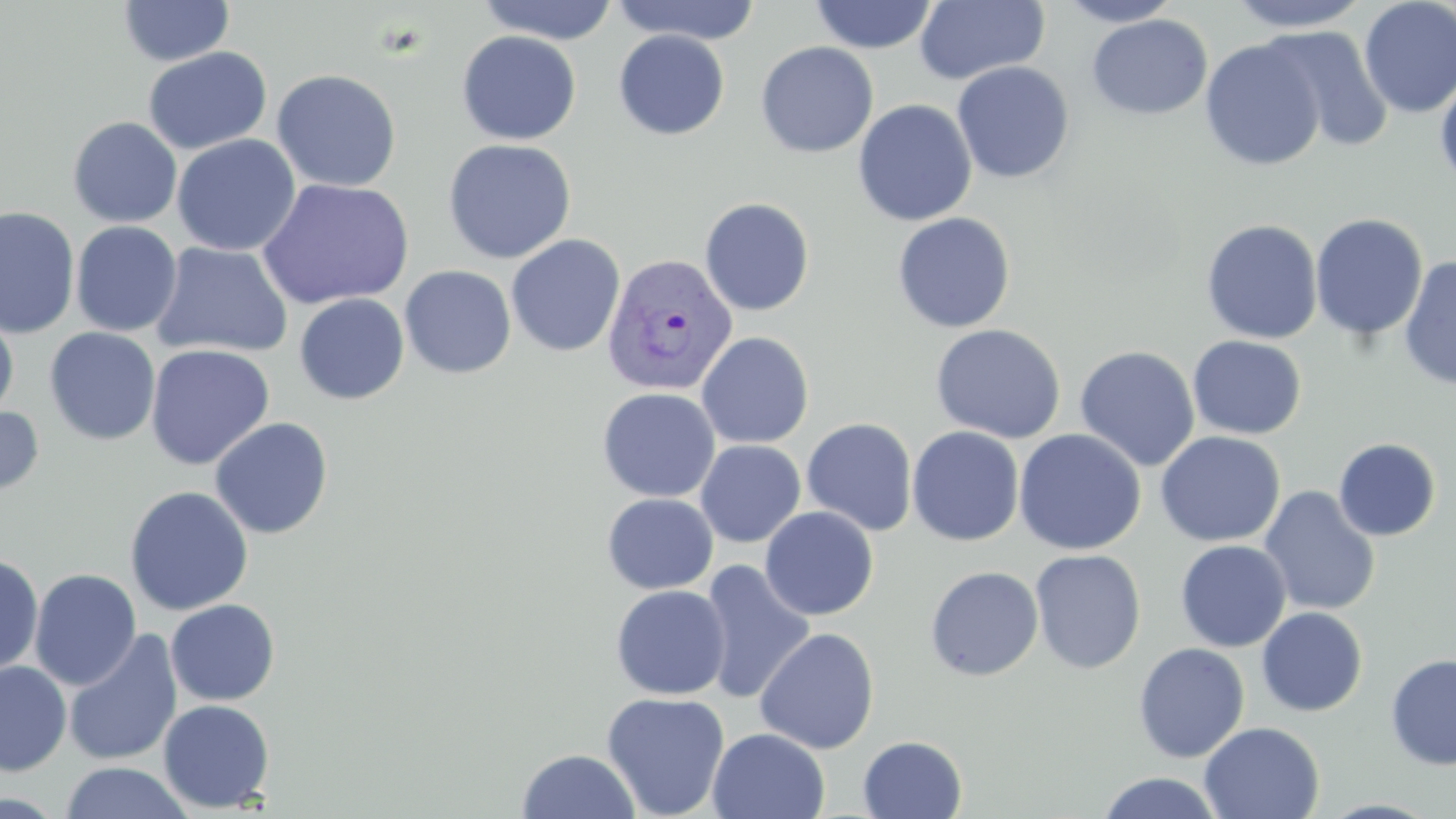 Approximate bounding boxes as (x1,y1)-(x2,y2) corner pairs in pixels. Plasmodium vivax-infected red blood cell locations: (601,251)-(738,397). Uninfected red blood cell locations: (477,0)-(620,45), (809,0)-(938,54), (913,0)-(1051,85), (1054,0)-(1185,27), (1224,0)-(1373,32), (1358,0)-(1456,118), (118,1)-(235,67), (608,1)-(762,45), (1087,14)-(1212,120), (1265,25)-(1394,152), (613,29)-(730,140), (456,30)-(581,146), (1199,38)-(1327,171), (755,41)-(879,158), (143,47)-(272,155), (952,61)-(1075,184), (271,68)-(402,192), (1434,73)-(1456,191), (852,99)-(978,227), (68,116)-(182,228), (172,134)-(300,256), (442,138)-(577,264), (257,178)-(414,310), (699,197)-(815,316), (0,206)-(80,338), (892,212)-(1016,333), (1310,213)-(1429,342), (1201,219)-(1323,344), (70,221)-(182,337), (505,234)-(626,357), (150,241)-(294,359), (1398,255)-(1456,390), (399,265)-(516,379), (294,293)-(410,405), (0,309)-(18,421), (930,323)-(1067,444), (44,328)-(161,445), (697,331)-(814,449), (1187,335)-(1307,440), (145,344)-(275,471), (1074,346)-(1200,472), (597,387)-(720,502), (0,404)-(44,500), (209,416)-(334,539), (802,418)-(917,536), (907,426)-(1025,546), (1014,429)-(1146,555), (1155,431)-(1285,547), (1333,438)-(1441,541), (695,440)-(806,547), (1259,485)-(1381,616), (124,486)-(253,616), (601,493)-(718,594), (760,506)-(879,621), (1175,539)-(1292,652), (1029,549)-(1146,674), (0,553)-(43,677), (698,560)-(816,704), (924,565)-(1044,681), (29,568)-(141,691), (610,584)-(731,700), (165,599)-(281,706), (1256,606)-(1368,716), (754,627)-(879,754), (62,629)-(183,767), (1133,642)-(1250,763), (1385,653)-(1456,770), (0,661)-(71,775), (601,692)-(730,819), (158,699)-(275,812), (1199,722)-(1325,818), (708,728)-(830,819), (858,735)-(967,818), (516,749)-(641,819), (59,762)-(195,819), (1094,772)-(1226,818). Slide-level diagnosis: Plasmodium vivax. May-Grünwald-Giemsa stain. Thin blood film. Image is 1456×819 pixels. Captured at 1000x magnification. Light microscopy. Single field of view.